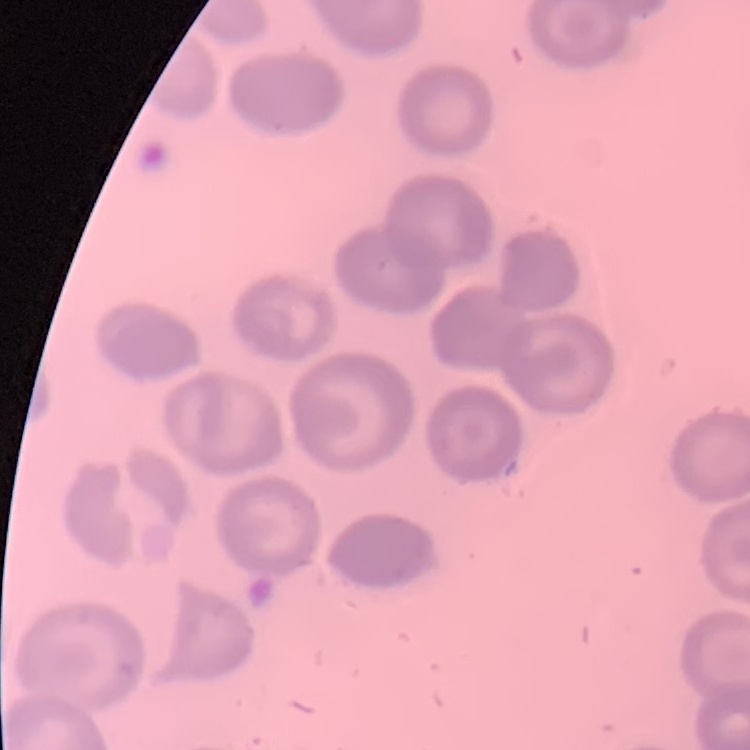
erythrocyte morphology = no rouleaux formation
stain = Field's or Giemsa
preparation = thin blood smear
image type = square crop of a larger photomicrograph